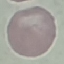
Summary:
  - Malaria status: uninfected
  - Stain: Giemsa
  - Preparation: thin blood film
  - Capture: smartphone through the microscope eyepiece
  - Image type: cell patch, automatically extracted from a larger field of view and resized to 64 × 64 pixels